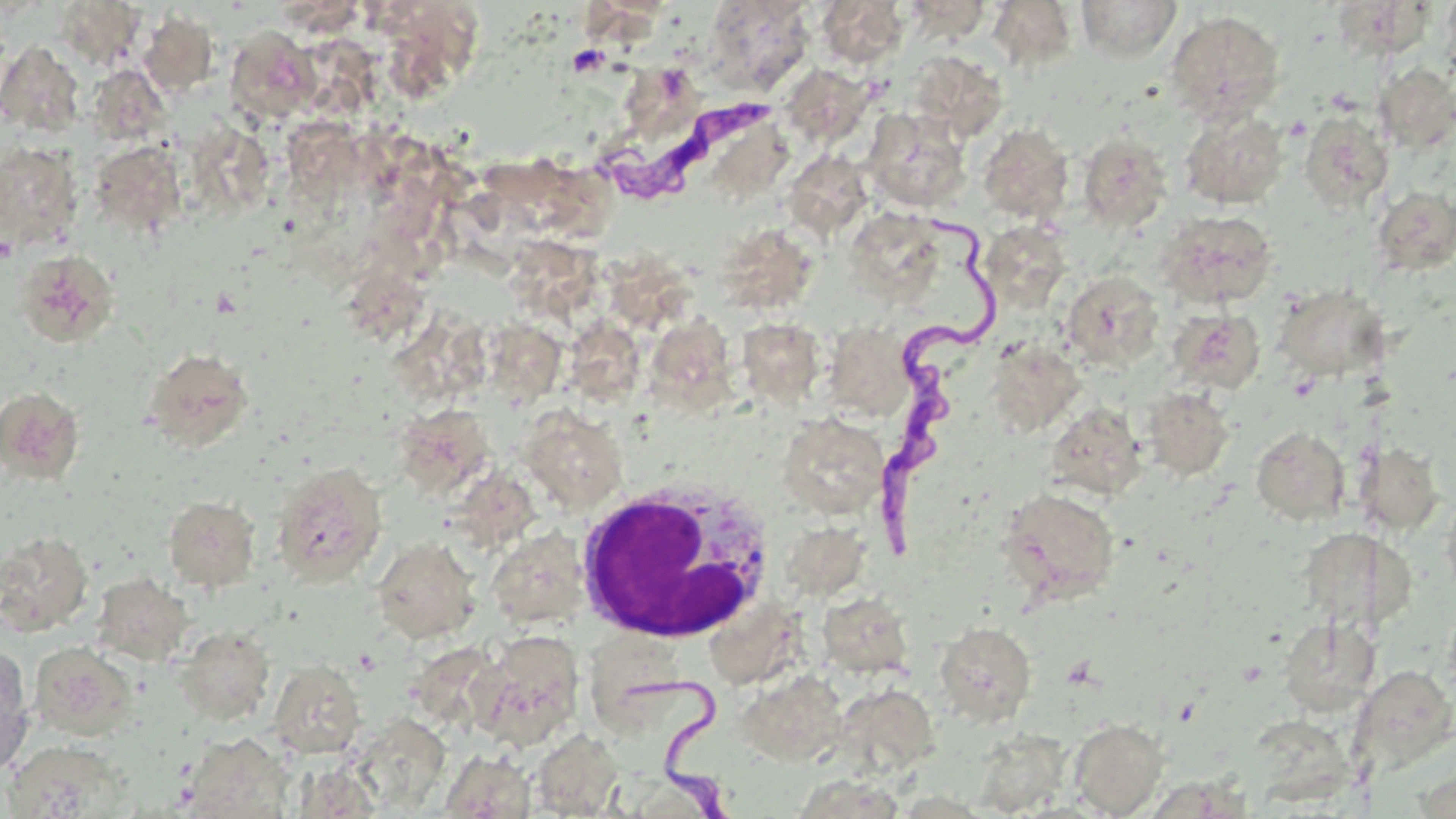
slide-level diagnosis = Trypanosoma brucei
stain = May-Grünwald-Giemsa
uninfected red blood cell locations = approximate bounding boxes as (x1,y1)-(x2,y2) corner pairs in pixels: (903,0)-(992,40), (1076,0)-(1182,62), (704,1)-(814,95), (817,1)-(908,68), (987,1)-(1079,71), (57,3)-(146,71), (139,11)-(219,98), (1166,11)-(1286,124), (383,13)-(495,103), (224,26)-(319,124), (0,41)-(84,137), (908,51)-(1007,142), (625,61)-(704,151), (1374,64)-(1456,154), (791,66)-(892,144), (96,72)-(181,139), (865,108)-(971,212), (1180,110)-(1289,209), (1299,110)-(1394,212), (192,117)-(273,212), (286,120)-(369,198), (977,123)-(1074,223), (1077,133)-(1172,231), (90,141)-(186,235), (0,143)-(82,252), (1371,186)-(1456,276), (843,207)-(949,310), (1157,210)-(1278,308), (995,220)-(1063,313), (727,227)-(808,316), (509,239)-(606,325), (594,244)-(694,333), (15,249)-(119,347), (1062,272)-(1164,369), (338,273)-(430,352), (1274,283)-(1391,382), (1168,309)-(1265,395), (398,312)-(496,414), (662,318)-(740,412), (735,318)-(825,408), (571,321)-(656,406), (825,323)-(915,419), (500,324)-(566,411), (989,339)-(1084,436), (143,347)-(254,452), (0,387)-(84,484), (1142,387)-(1235,481), (412,401)-(493,498), (1045,403)-(1148,501), (521,407)-(628,512), (778,413)-(889,517), (1252,427)-(1349,523), (1356,441)-(1444,535), (272,462)-(387,587), (454,466)-(548,556), (1000,487)-(1120,604), (1442,488)-(1456,602), (164,495)-(260,592), (783,522)-(863,607), (0,530)-(93,635), (493,534)-(591,636), (1306,536)-(1410,631), (372,537)-(480,643), (91,573)-(193,666), (816,591)-(915,679), (720,597)-(815,706), (1268,619)-(1371,706), (934,621)-(1037,725), (174,626)-(276,724), (469,630)-(586,750), (29,642)-(137,740), (0,645)-(35,775), (268,660)-(366,759), (1347,662)-(1456,770), (737,671)-(849,765), (832,683)-(941,777), (359,714)-(456,813), (1247,715)-(1346,813), (1068,718)-(1169,817), (530,729)-(625,817), (971,729)-(1070,818), (181,732)-(293,819), (3,740)-(130,818), (440,750)-(536,818)
modality = optical microscopy
field of view = one of a larger specimen
preparation = thin blood smear
platelet locations = approximate bounding boxes as (x1,y1)-(x2,y2) corner pairs in pixels: (567,45)-(609,76)
magnification = 1000x
image size = 1456×819 pixels
white blood cell locations = approximate bounding boxes as (x1,y1)-(x2,y2) corner pairs in pixels: (573,480)-(776,642)
Trypanosoma brucei locations = approximate bounding boxes as (x1,y1)-(x2,y2) corner pairs in pixels: (601,89)-(776,202), (788,156)-(883,249), (870,215)-(992,569), (611,670)-(727,819)